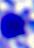
Micrograph. A leukocyte is shown. Captured at 400x magnification.